Locate every blood parasite and identify its species.
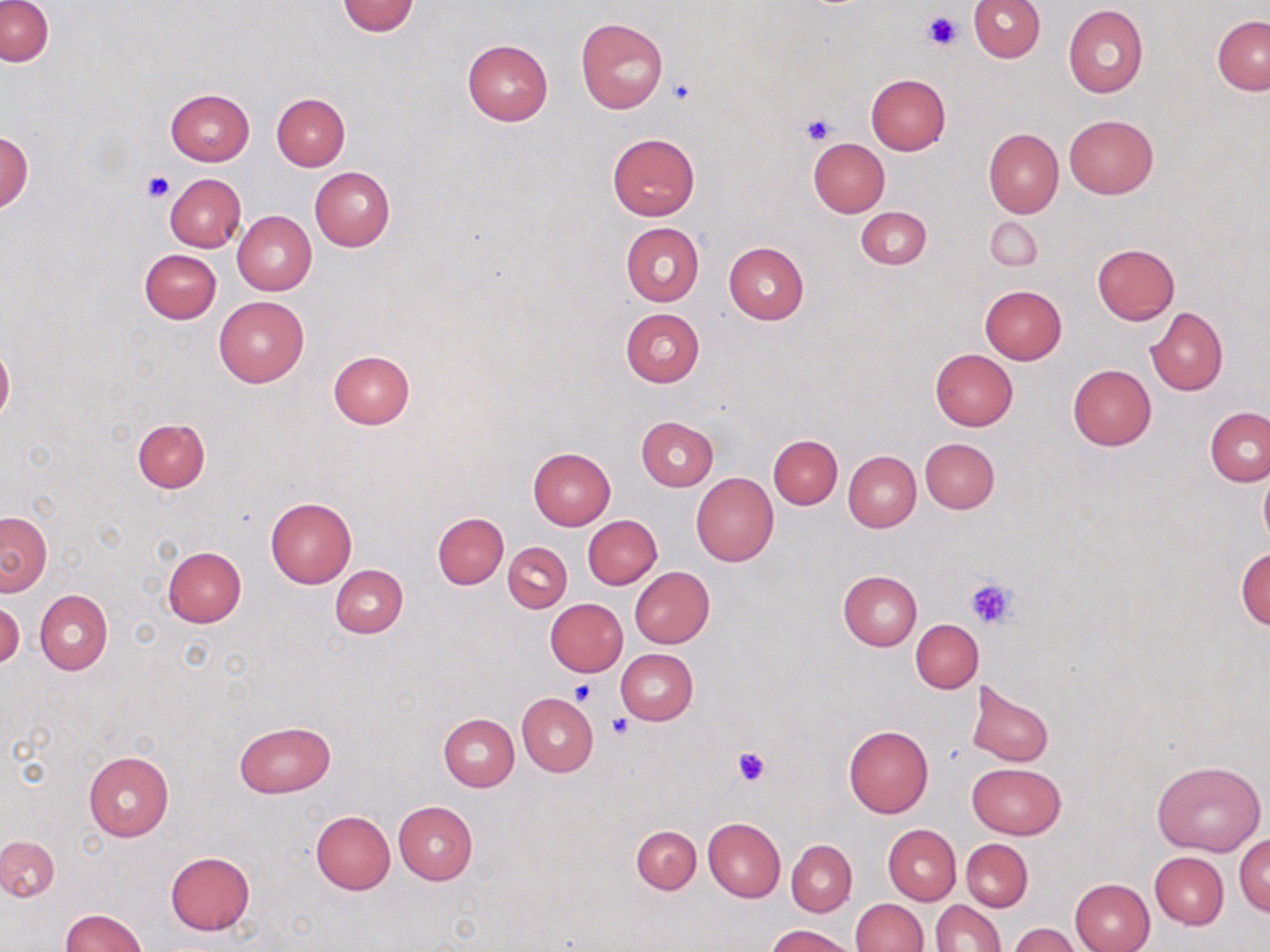
No blood parasites seen.

Summary:
  - Coordinate format: approximate bounding boxes as (x1,y1)-(x2,y2) corner pairs in pixels
  - Platelet locations: (922,11)-(959,50), (668,80)-(695,105), (801,112)-(837,146), (141,169)-(173,203), (964,579)-(1016,627), (568,679)-(597,707), (608,713)-(634,739), (734,746)-(773,788)
  - Uninfected red blood cell locations: (969,0)-(1045,62), (1,1)-(53,67), (337,1)-(419,36), (1064,5)-(1148,98), (1212,15)-(1270,95), (576,17)-(668,113), (462,40)-(553,125), (866,74)-(950,155), (165,88)-(255,165), (271,93)-(350,171), (1064,115)-(1158,198), (984,128)-(1063,219), (0,131)-(32,211), (607,133)-(699,220), (808,137)-(890,217), (310,167)-(394,251), (164,174)-(246,252), (855,207)-(931,269), (232,210)-(316,294), (984,216)-(1041,271), (621,223)-(704,306), (724,242)-(808,323), (1092,244)-(1180,323), (139,248)-(221,323), (979,284)-(1067,365), (213,295)-(310,387), (1146,307)-(1227,395), (621,308)-(704,386), (0,342)-(14,422), (327,349)-(416,430), (929,349)-(1017,431), (1068,365)-(1157,450), (1205,408)-(1270,485), (636,416)-(718,490), (132,419)-(210,493), (768,434)-(842,509), (920,438)-(998,513), (528,447)-(616,529), (844,451)-(921,532), (1259,464)-(1270,551), (691,473)-(778,566), (265,497)-(358,589), (1,511)-(51,595), (433,512)-(509,588), (584,515)-(662,588), (504,542)-(572,612), (162,546)-(247,627), (1235,546)-(1270,629), (331,564)-(408,638), (629,567)-(714,648), (837,570)-(922,651), (35,590)-(112,674), (546,598)-(627,676), (0,600)-(24,670), (912,619)-(984,693), (615,649)-(698,725), (965,681)-(1052,768), (518,693)-(598,777), (439,714)-(519,790), (234,722)-(335,797), (843,725)-(934,818), (83,751)-(173,841), (1152,759)-(1264,855), (967,763)-(1066,838), (393,800)-(478,885), (310,811)-(395,893), (703,818)-(785,901), (883,824)-(961,905), (632,825)-(701,894), (1235,833)-(1270,916), (0,835)-(59,901), (961,839)-(1032,911), (787,840)-(857,915), (166,851)-(255,934), (1150,851)-(1227,928), (1070,878)-(1155,952), (851,899)-(928,952), (932,900)-(1004,951), (59,910)-(148,952), (768,924)-(855,952), (1008,925)-(1083,952)
  - Slide-level diagnosis: negative for blood parasites
  - Stain: May-Grünwald-Giemsa
  - Modality: light microscopy
  - Magnification: 1000x
  - Field of view: one of a larger specimen
  - Image size: 1270×952 pixels
  - Preparation: thin blood smear